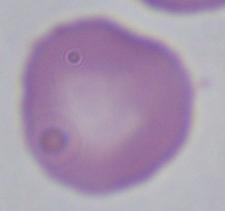

{
  "identification": "Babesia",
  "magnification": "1000x",
  "modality": "photomicrograph"
}